Classify the preparation.
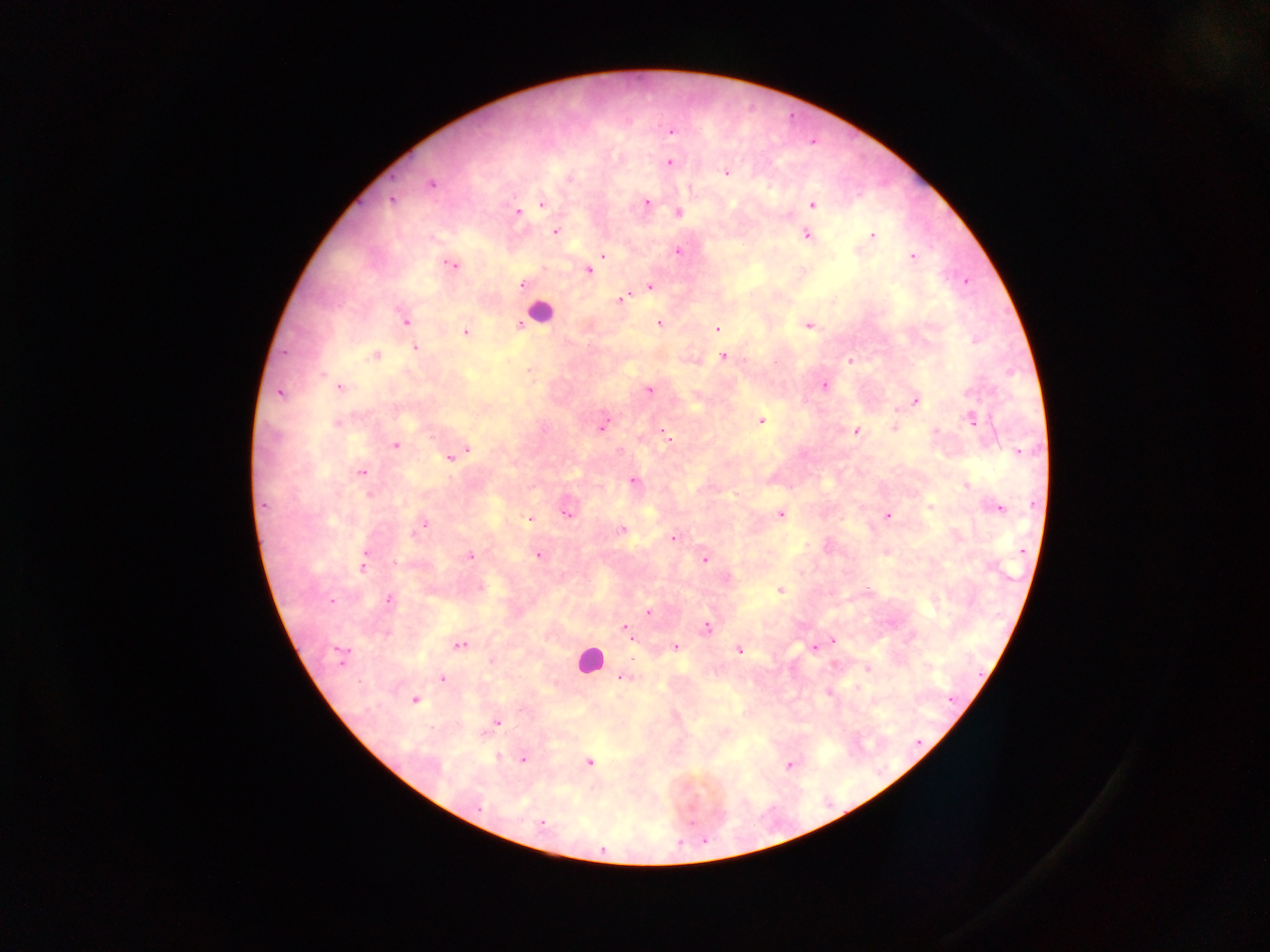

Thick blood smear.

{
  "malaria_parasite_locations": "approximate centers as (x, y) in pixels: (671, 131), (671, 163), (726, 173), (569, 178), (431, 184), (392, 200), (647, 202), (542, 204), (812, 204), (518, 212), (678, 213), (556, 231), (872, 235), (807, 236), (678, 251), (603, 255), (912, 257), (450, 264), (589, 271), (967, 281), (523, 286), (650, 287), (621, 299), (405, 321), (659, 323), (519, 324), (807, 326), (717, 329), (465, 332), (975, 341), (415, 348), (375, 355), (723, 356), (851, 360), (324, 374), (824, 386), (340, 387), (649, 390), (279, 394), (916, 402), (761, 420), (971, 420), (337, 423), (603, 425), (894, 428), (856, 431), (666, 434), (396, 445), (468, 449), (1019, 452), (450, 458), (362, 472), (634, 481), (967, 484), (368, 495), (264, 506), (929, 507), (999, 508), (566, 514), (780, 515), (887, 516), (529, 519), (423, 525), (419, 529), (621, 530), (673, 538), (470, 556), (538, 556), (704, 559), (396, 563), (363, 564), (481, 587), (780, 589), (867, 591), (389, 600), (332, 601), (648, 611), (706, 627), (625, 628), (832, 641), (460, 644), (676, 647), (814, 648), (738, 650), (342, 652), (633, 658), (868, 669), (623, 677), (442, 679), (952, 699), (415, 700), (498, 722), (498, 757), (523, 759), (589, 762), (790, 764), (479, 807), (542, 824)",
  "field_of_view": "single",
  "capture": "mobile-phone photograph through a microscope",
  "leukocyte_locations": "approximate centers as (x, y) in pixels: (539, 312), (589, 659)",
  "country": "Ghana",
  "image_size": "1270×952 pixels"
}